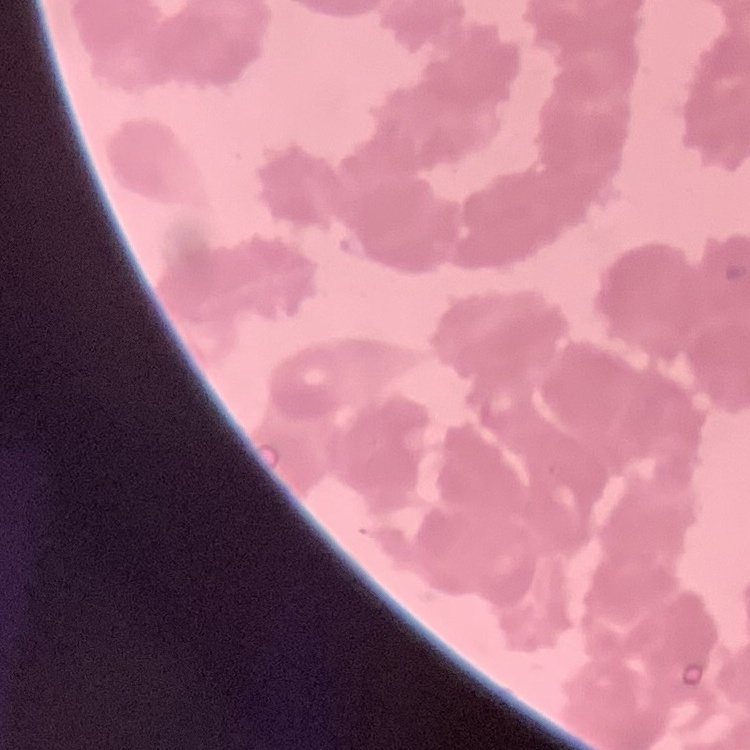

red blood cell morphology = rouleaux formation
stain = Field's or Giemsa
image type = square crop of a larger photomicrograph
preparation = thin peripheral smear